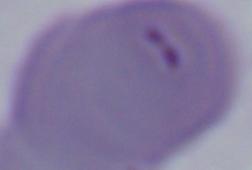 Micrograph. A Babesia parasite is shown. Captured at 1000x magnification.